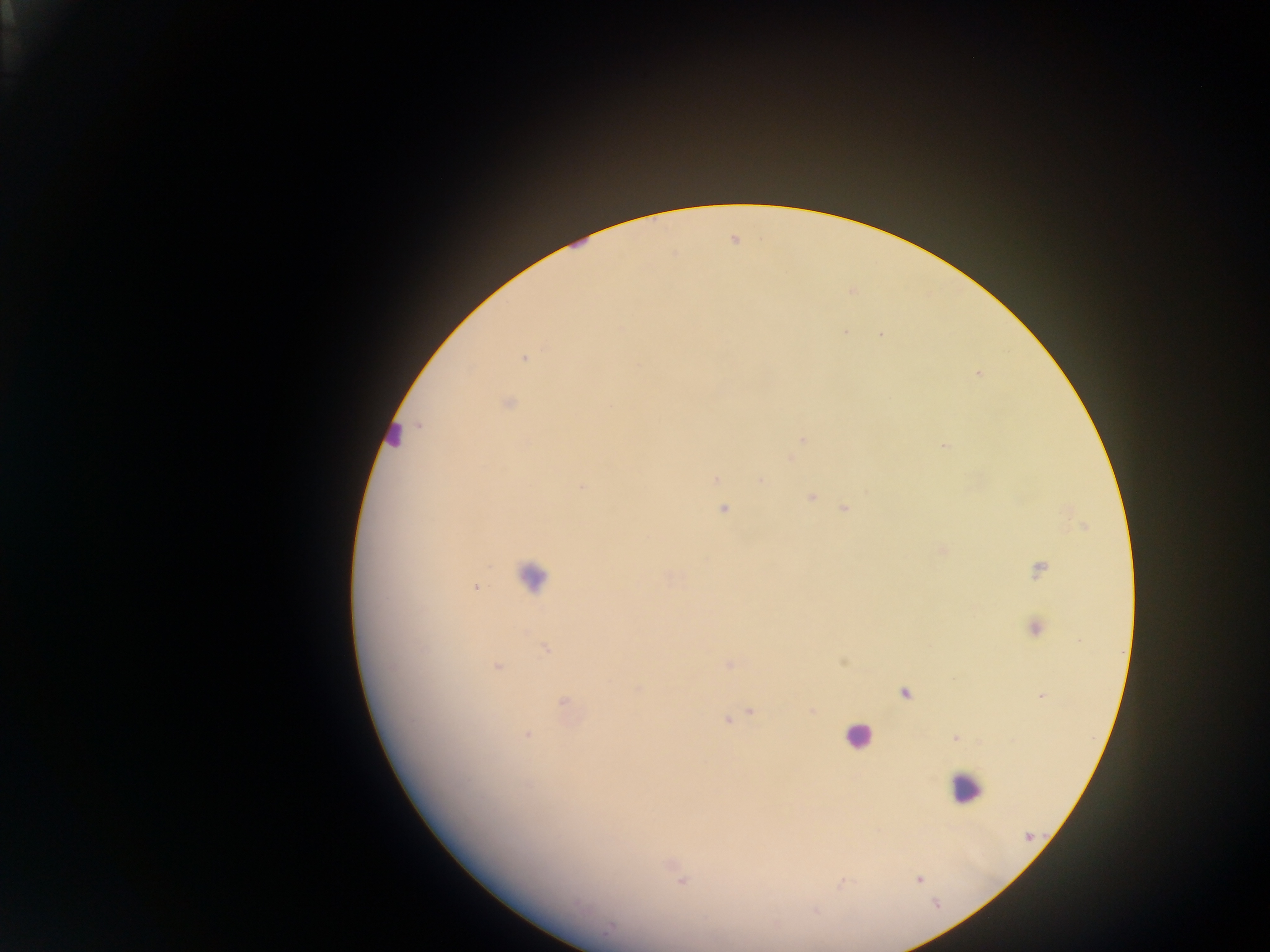
malaria_parasite_locations: 'approximate centers as (x, y) in pixels: (845, 333), (881, 334), (524, 358), (979, 373), (507, 404), (803, 439), (945, 446), (717, 479), (761, 481), (583, 486), (811, 498), (844, 508), (724, 509), (1039, 570), (475, 588), (1034, 629), (546, 648), (842, 662), (729, 664), (391, 667), (497, 667), (638, 690), (904, 693), (1042, 697), (563, 701), (751, 711), (727, 720), (526, 735), (955, 738), (1028, 836), (919, 879), (682, 881), (609, 929)'
preparation: thick blood smear
leukocyte_locations: 'approximate centers as (x, y) in pixels: (392, 432), (531, 575), (857, 736), (965, 787)'
country: Ghana
field_of_view: single
capture: mobile-phone photograph through a microscope
image_size: 1270×952 pixels